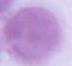 Micrograph. An erythrocyte is seen. 1000x magnification.